Locate malaria parasites and leukocytes.
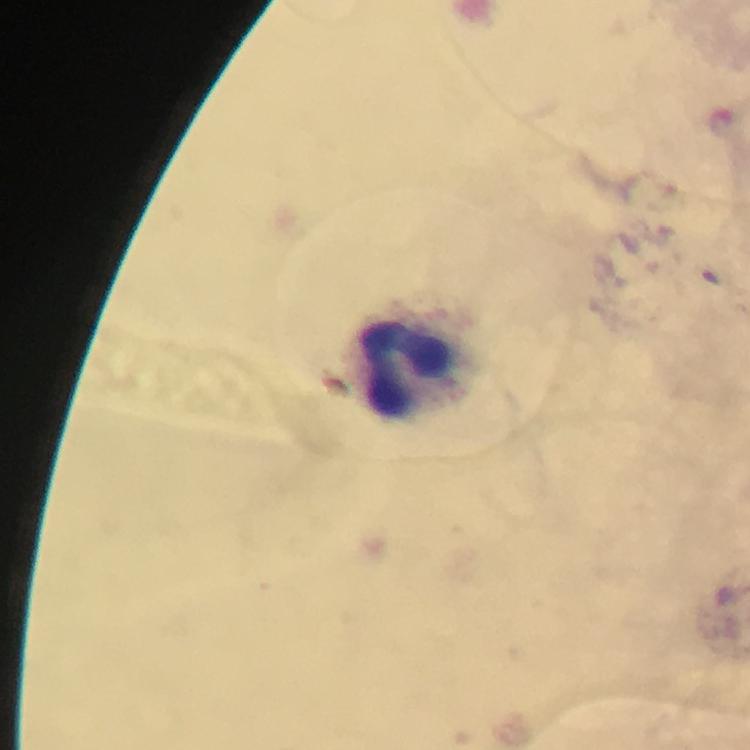

No malaria parasites detected.
Approximate centers as {x, y} in pixels.
Leukocytes: {409, 368}.

image size = 750×750 pixels
cropped from = one field of view
magnification = 100x
context = from a malaria diagnostic workup
immersion oil = used
stain = Giemsa
capture = smartphone photograph through a microscope
preparation = thick smear